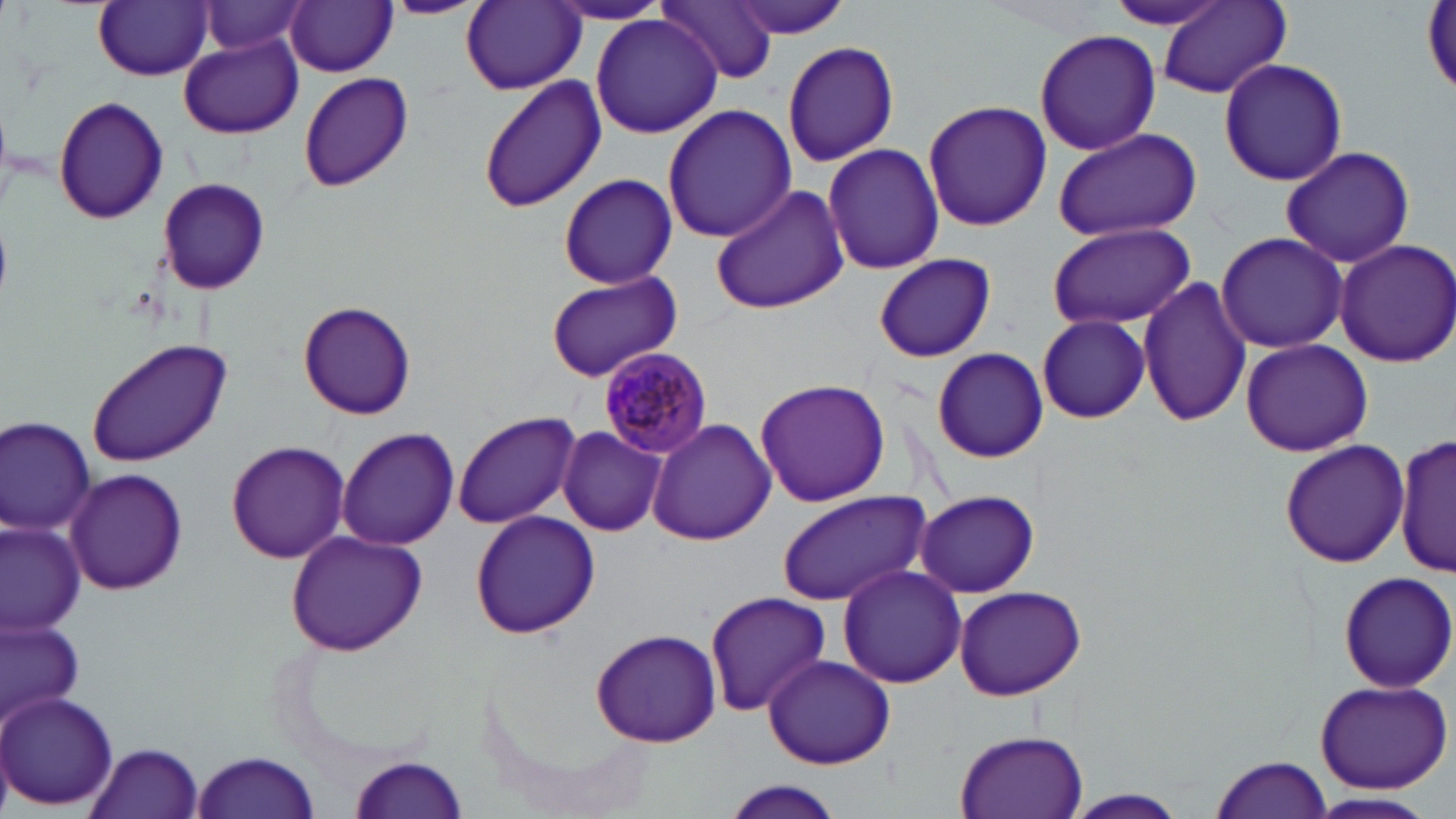

Approximate bounding boxes as (x1,y1)-(x2,y2) corner pairs in pixels. Uninfected red blood cell locations: (379,0)-(487,18), (658,0)-(776,85), (729,0)-(854,40), (94,1)-(212,81), (285,1)-(398,76), (462,1)-(585,93), (1101,1)-(1240,32), (1159,1)-(1289,100), (199,2)-(315,60), (545,2)-(674,26), (1422,3)-(1456,95), (590,13)-(724,137), (1033,28)-(1162,157), (179,37)-(301,138), (782,41)-(898,168), (1217,58)-(1349,186), (299,70)-(414,192), (479,78)-(606,213), (52,95)-(171,224), (922,99)-(1053,231), (662,103)-(797,243), (1050,127)-(1203,242), (822,142)-(946,275), (1280,144)-(1415,268), (556,173)-(682,287), (157,177)-(269,295), (709,185)-(848,315), (1044,222)-(1196,329), (1214,232)-(1349,354), (1332,239)-(1456,368), (872,254)-(997,363), (545,270)-(681,381), (1138,274)-(1250,428), (298,300)-(416,420), (1037,313)-(1150,423), (87,337)-(230,466), (1240,338)-(1373,457), (932,346)-(1048,464), (754,378)-(891,505), (451,411)-(581,530), (0,414)-(96,535), (649,419)-(775,544), (557,426)-(666,536), (337,427)-(459,549), (1395,434)-(1454,579), (1278,438)-(1410,570), (227,441)-(349,563), (65,467)-(188,596), (915,489)-(1039,598), (775,491)-(925,606), (471,509)-(600,639), (1,521)-(85,635), (283,531)-(428,656), (836,563)-(965,688), (1337,570)-(1456,692), (951,584)-(1087,700), (705,592)-(831,717), (0,614)-(84,727), (590,629)-(721,748), (763,653)-(895,770), (1313,679)-(1454,794), (0,690)-(119,812), (954,727)-(1091,819), (86,742)-(205,819), (193,750)-(320,819), (352,753)-(469,818), (1212,755)-(1332,819), (715,781)-(849,818), (1062,789)-(1192,818), (1307,792)-(1438,817). Plasmodium malariae-infected red blood cell locations: (598,347)-(712,458). Slide-level diagnosis: Plasmodium malariae. May-Grünwald-Giemsa-stained preparation. Captured at 1000x magnification. Thin blood smear. Image is 1456×819 pixels. One field of a larger specimen. Optical microscopy.